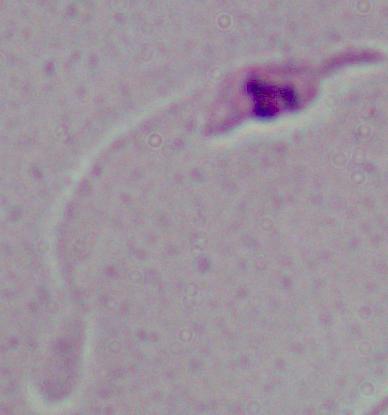
Summary:
  - Magnification: 1000x
  - Identification: Leishmania
  - Modality: micrograph